Give the extent of all uninfected red blood cells.
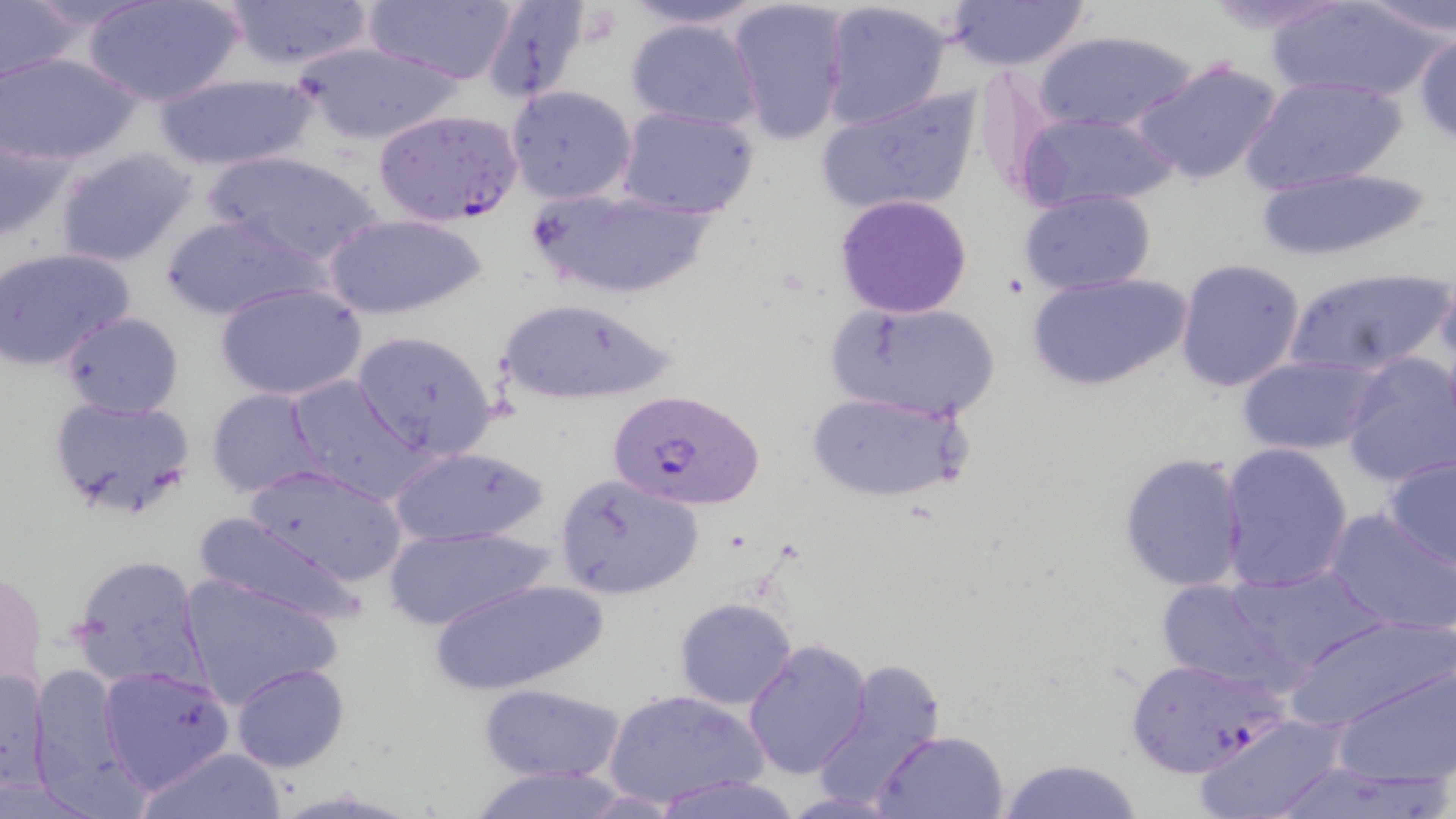
Approximate bounding boxes as named x1/y1/x2/y2 corners in pixels.
Uninfected red blood cells: (x1=218, y1=0, x2=377, y2=70), (x1=363, y1=0, x2=521, y2=87), (x1=479, y1=0, x2=595, y2=107), (x1=614, y1=0, x2=775, y2=31), (x1=940, y1=0, x2=1095, y2=70), (x1=1195, y1=0, x2=1359, y2=37), (x1=1357, y1=0, x2=1455, y2=40), (x1=0, y1=1, x2=82, y2=82), (x1=85, y1=1, x2=245, y2=107), (x1=729, y1=1, x2=849, y2=146), (x1=1266, y1=1, x2=1449, y2=103), (x1=819, y1=2, x2=954, y2=130), (x1=623, y1=15, x2=766, y2=133), (x1=1031, y1=30, x2=1201, y2=135), (x1=1413, y1=32, x2=1456, y2=146), (x1=287, y1=39, x2=470, y2=147), (x1=0, y1=51, x2=143, y2=165), (x1=1133, y1=57, x2=1287, y2=188), (x1=149, y1=71, x2=321, y2=171), (x1=1241, y1=76, x2=1408, y2=195), (x1=505, y1=85, x2=636, y2=204), (x1=814, y1=88, x2=983, y2=219), (x1=616, y1=106, x2=761, y2=219), (x1=1015, y1=111, x2=1183, y2=214), (x1=0, y1=126, x2=77, y2=243), (x1=55, y1=146, x2=198, y2=268), (x1=204, y1=149, x2=388, y2=269), (x1=1246, y1=164, x2=1436, y2=262), (x1=526, y1=183, x2=717, y2=302), (x1=1018, y1=189, x2=1159, y2=296), (x1=833, y1=194, x2=975, y2=318), (x1=158, y1=212, x2=327, y2=321), (x1=324, y1=212, x2=485, y2=320), (x1=0, y1=248, x2=135, y2=372), (x1=1174, y1=257, x2=1307, y2=394), (x1=1284, y1=264, x2=1452, y2=381), (x1=1025, y1=271, x2=1193, y2=393), (x1=215, y1=280, x2=368, y2=401), (x1=493, y1=295, x2=682, y2=407), (x1=826, y1=300, x2=1003, y2=423), (x1=60, y1=312, x2=183, y2=419), (x1=351, y1=330, x2=500, y2=461), (x1=1338, y1=351, x2=1455, y2=489), (x1=1235, y1=355, x2=1378, y2=455), (x1=282, y1=375, x2=426, y2=501), (x1=205, y1=388, x2=327, y2=497), (x1=805, y1=391, x2=970, y2=504), (x1=45, y1=394, x2=196, y2=521), (x1=1218, y1=443, x2=1355, y2=593), (x1=386, y1=444, x2=551, y2=548), (x1=1118, y1=451, x2=1249, y2=592), (x1=1380, y1=452, x2=1456, y2=572), (x1=243, y1=464, x2=408, y2=586), (x1=555, y1=474, x2=704, y2=600), (x1=1325, y1=508, x2=1456, y2=635), (x1=192, y1=512, x2=366, y2=632), (x1=381, y1=523, x2=552, y2=632), (x1=68, y1=554, x2=205, y2=691), (x1=1216, y1=562, x2=1389, y2=680), (x1=1, y1=567, x2=47, y2=699), (x1=178, y1=572, x2=341, y2=707), (x1=424, y1=576, x2=610, y2=698), (x1=1153, y1=579, x2=1300, y2=691), (x1=673, y1=596, x2=798, y2=710), (x1=1281, y1=614, x2=1453, y2=735), (x1=742, y1=638, x2=873, y2=779), (x1=815, y1=659, x2=955, y2=804), (x1=1334, y1=659, x2=1454, y2=787), (x1=230, y1=662, x2=350, y2=773), (x1=28, y1=663, x2=141, y2=813), (x1=101, y1=664, x2=235, y2=792), (x1=1, y1=666, x2=52, y2=794), (x1=479, y1=682, x2=626, y2=783), (x1=604, y1=687, x2=767, y2=809), (x1=1192, y1=714, x2=1348, y2=819), (x1=873, y1=728, x2=1010, y2=818), (x1=132, y1=746, x2=289, y2=819), (x1=997, y1=758, x2=1148, y2=819), (x1=465, y1=765, x2=634, y2=819), (x1=651, y1=772, x2=806, y2=819).

{
  "slide_level_diagnosis": "Plasmodium falciparum",
  "stain": "May-Grünwald-Giemsa",
  "magnification": "1000x",
  "plasmodium_falciparum_infected_red_blood_cell_locations": "approximate bounding boxes as named x1/y1/x2/y2 corners in pixels: (x1=375, y1=108, x2=523, y2=227), (x1=605, y1=388, x2=766, y2=511), (x1=1121, y1=656, x2=1290, y2=779)",
  "preparation": "thin blood smear",
  "field_of_view": "one of a larger specimen",
  "modality": "optical microscopy",
  "image_size": "1456×819 pixels"
}